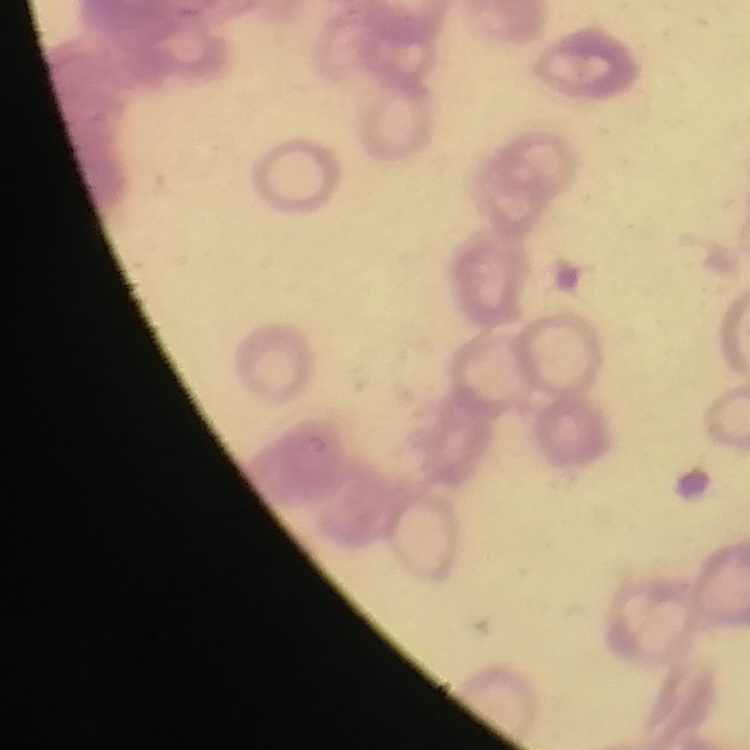
The erythrocytes show rouleaux formation. Thin peripheral smear. Stained with either Field's or Giemsa. Square crop of a larger photomicrograph.